Assess the morphology of the red blood cells.
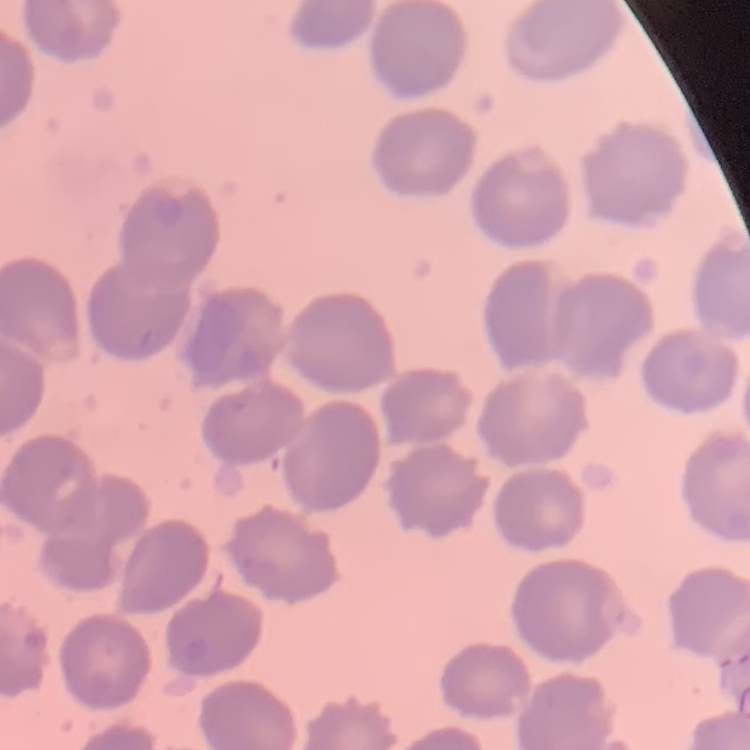
No rouleaux formation.

image_type: one tile cut from a larger photomicrograph
preparation: thin blood smear
stain: Field's or Giemsa